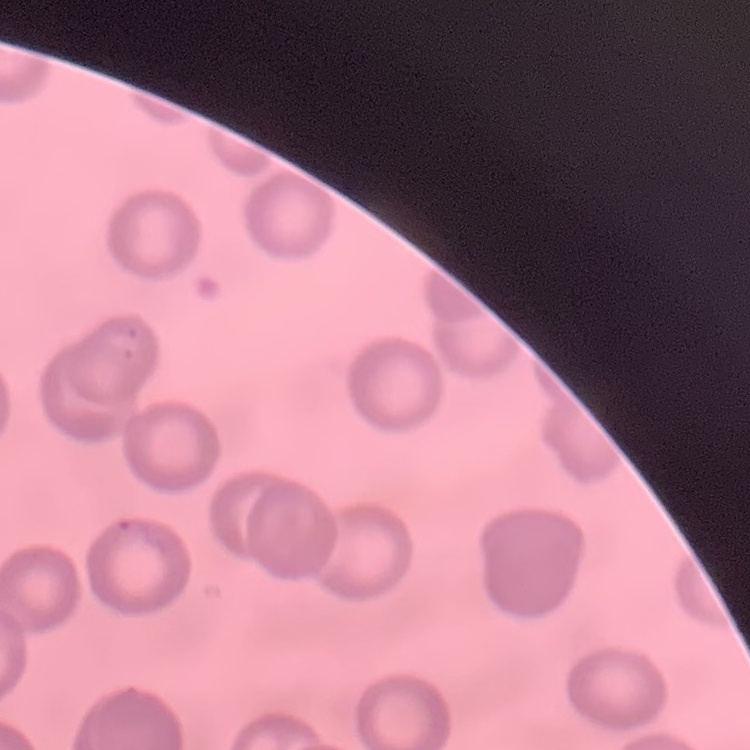
Summary:
  - Red blood cell morphology: no rouleaux formation
  - Stain: Field's or Giemsa
  - Image type: one tile cut from a larger photomicrograph
  - Preparation: thin blood film